Assess this cell for malaria.
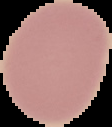

It is uninfected.

From a thin blood film. Segmented cell region on a black background. Image is 112×127 pixels.